State which parasite is depicted.
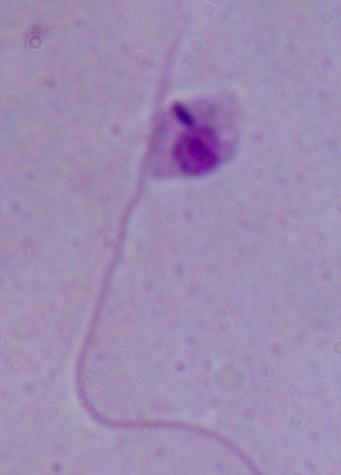

Leishmania.

Summary:
  - Modality: photomicrograph
  - Magnification: 1000x